Identify the preparation type.
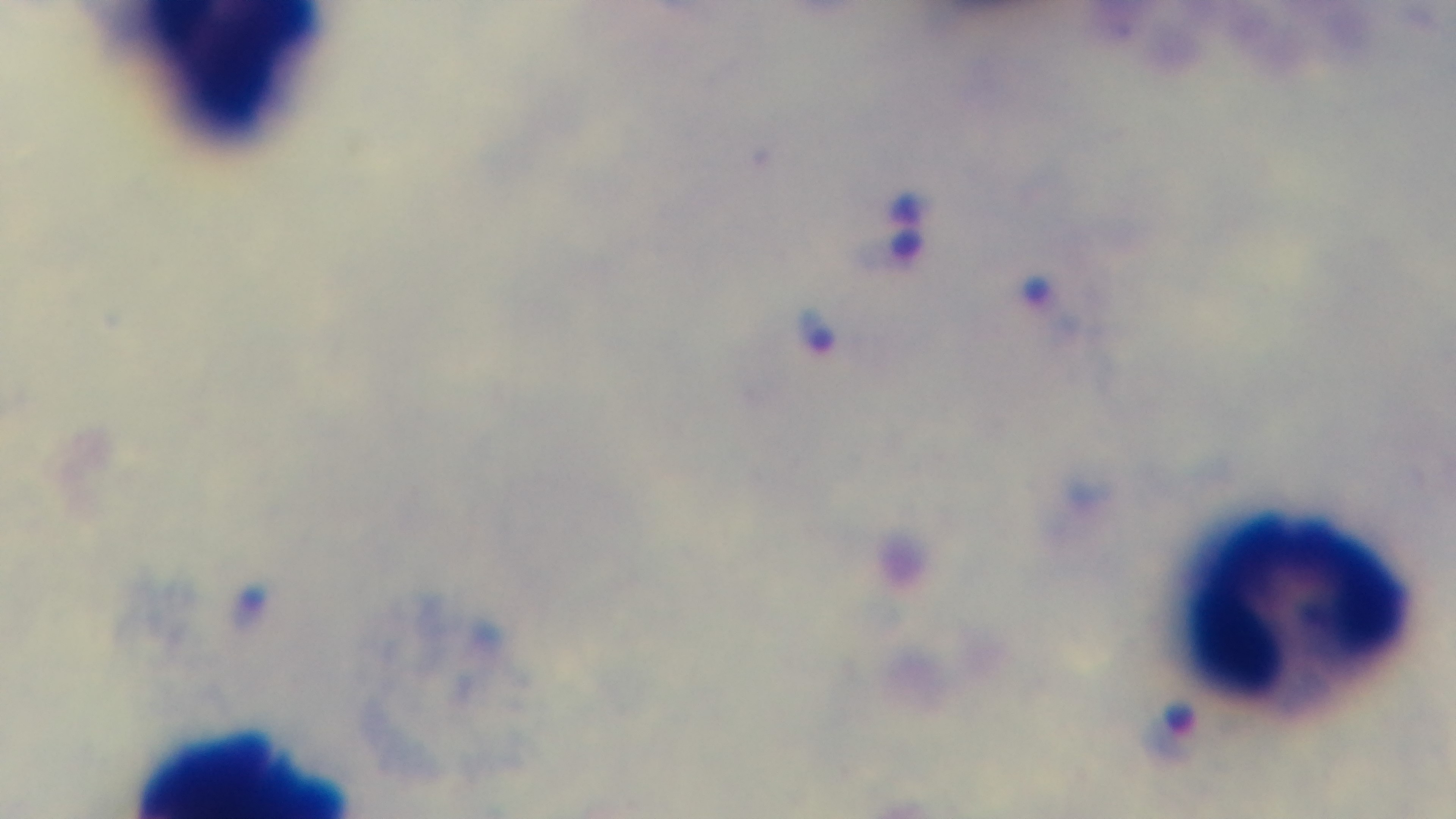

A thick smear.

Single field of view. Photomicrograph. Oil-immersion objective, 100x. Captured with a mounted 4K digital camera. Malaria status: positive. Giemsa stain.